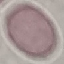
Summary:
  - Malaria status: uninfected
  - Capture: smartphone through the microscope eyepiece
  - Stain: Giemsa
  - Preparation: thin blood film
  - Image type: automatically extracted cell patch, resized to 64 × 64 pixels